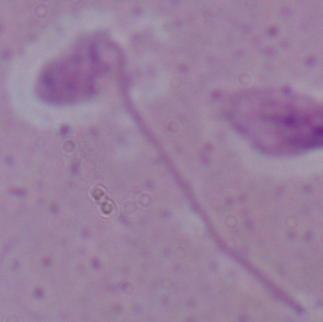
{
  "magnification": "1000x",
  "modality": "photomicrograph",
  "identification": "Leishmania"
}